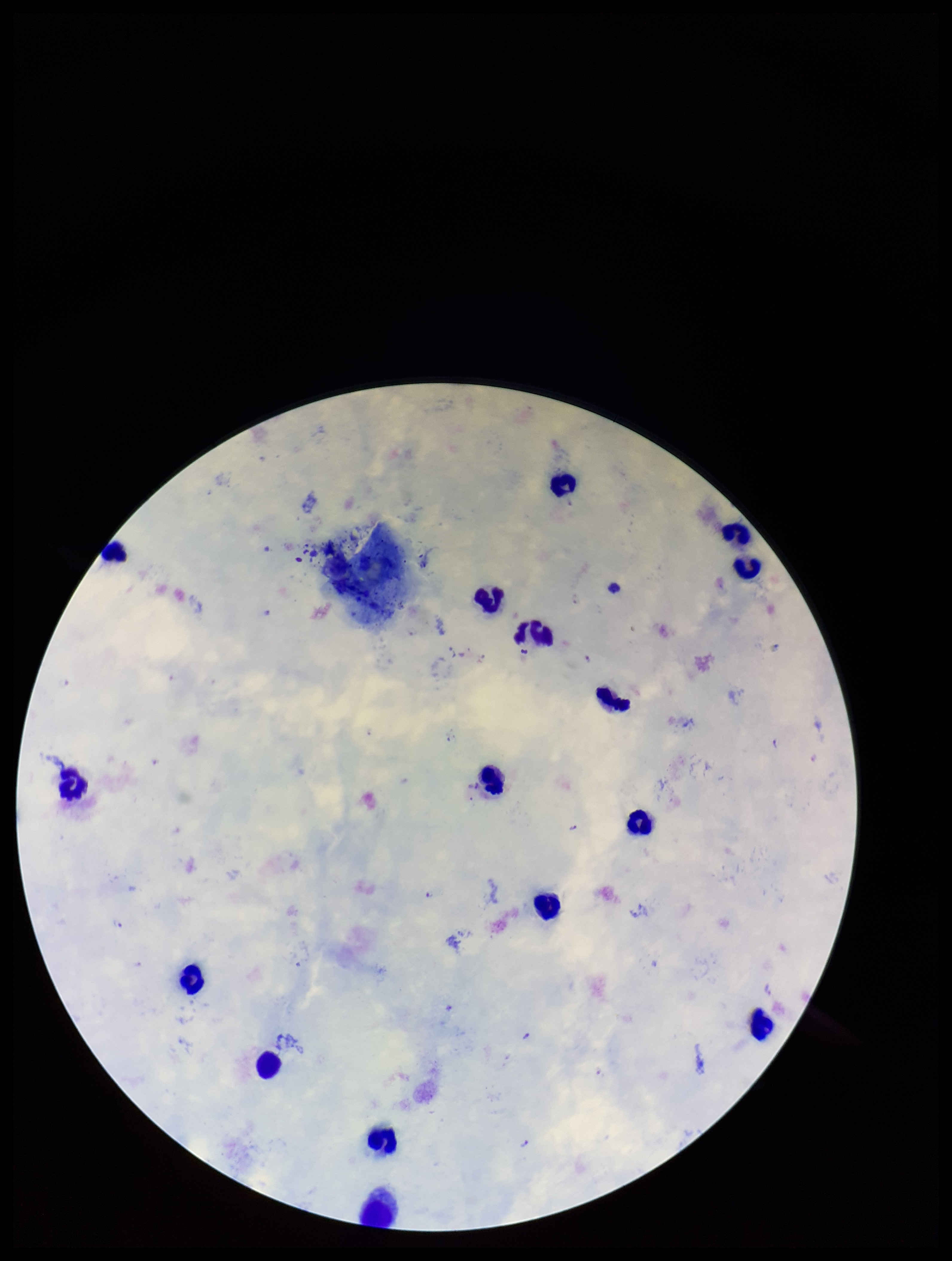 Single field of view. Preparation: thick smear. Stained with Giemsa. Leukocyte count: 16. Image is 952×1261 pixels. Plasmodium parasites: seen. Photographed through the microscope eyepiece with a smartphone camera. Species reported for this patient: Plasmodium falciparum. Parasite count: 7. Patient malaria status: infected.